Classify this cell by malaria status.
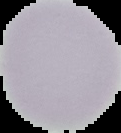

Uninfected.

Summary:
  - Image type: segmented cell region on a black background
  - Preparation: thin blood film
  - Image size: 121×133 pixels